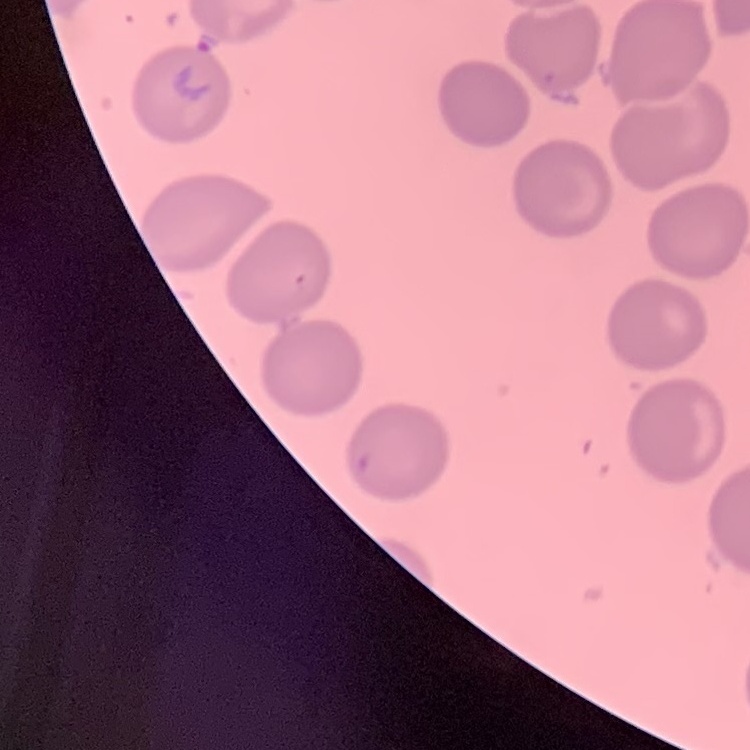

erythrocyte_morphology: no rouleaux formation
preparation: thin blood film
stain: Field's or Giemsa
image_type: square crop of a larger photomicrograph